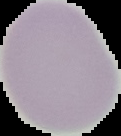

Summary:
  - Image size: 121×136 pixels
  - Preparation: thin blood film
  - Malaria status: uninfected
  - Image type: segmented cell region with the area outside set to black